Assess this cell for malaria.
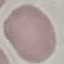

Uninfected.

preparation = thin blood smear
capture = smartphone through the microscope eyepiece
stain = Giemsa
image type = cell patch, automatically extracted from a larger field of view and resized to 64 × 64 pixels